Report the malaria status of this cell.
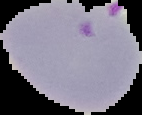

It is parasitized.

Image is 142×115 pixels. Segmented cell region on a black background. From a thin blood film.